Identify the blood parasite species.
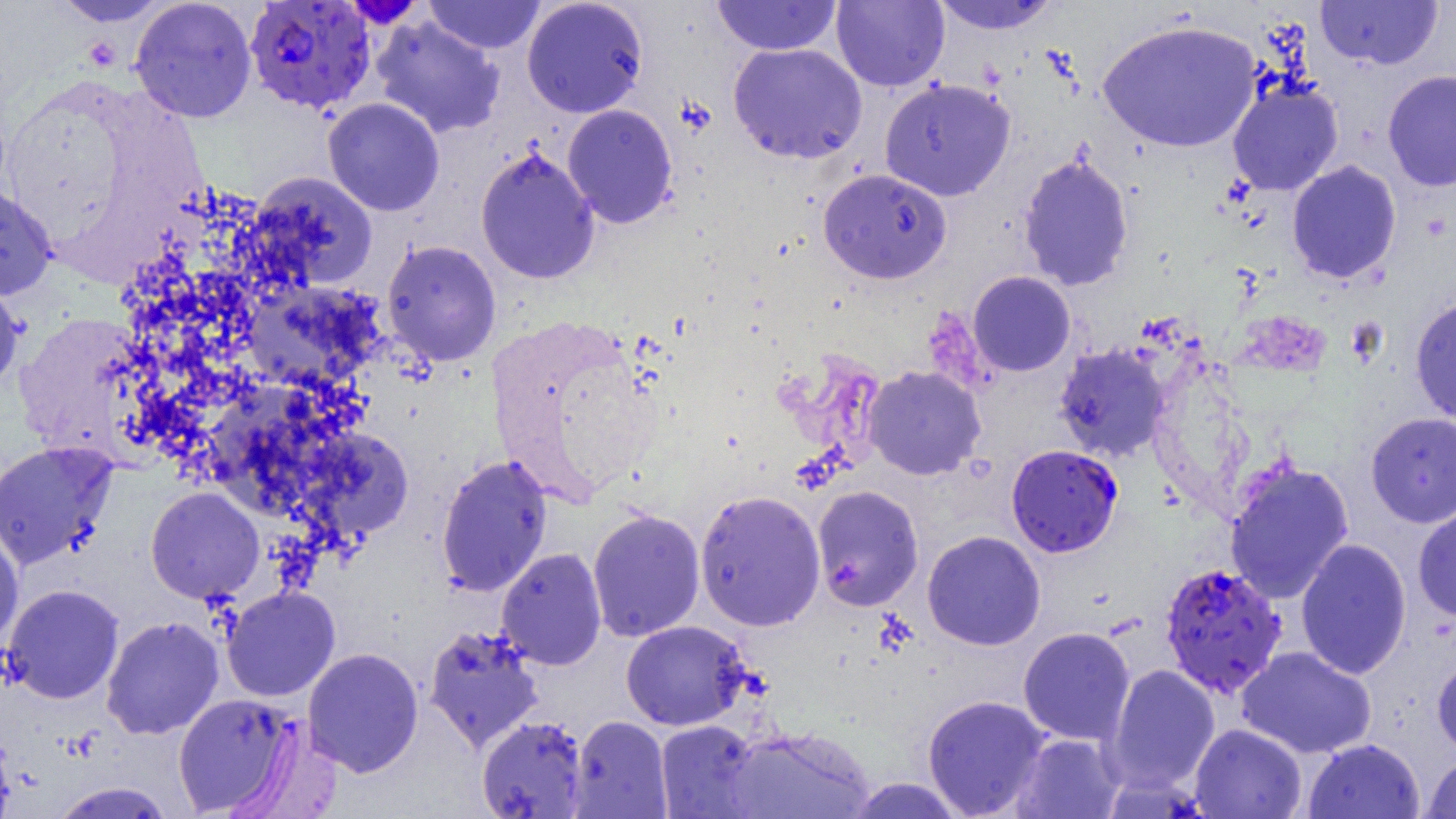

Plasmodium falciparum.

Approximate bounding boxes as (x1,y1)-(x2,y2) corner pairs in pixels. Uninfected red blood cell locations: (51,0)-(172,26), (424,0)-(546,54), (521,0)-(649,118), (711,0)-(842,56), (831,0)-(949,91), (930,0)-(1061,35), (1315,0)-(1443,69), (130,1)-(257,123), (371,16)-(505,138), (1097,19)-(1262,153), (728,43)-(868,164), (1382,70)-(1456,192), (879,77)-(1015,201), (1227,78)-(1343,196), (322,98)-(445,216), (562,104)-(678,228), (475,147)-(600,284), (1017,152)-(1135,292), (1286,160)-(1402,284), (818,168)-(952,283), (249,171)-(378,290), (0,184)-(56,301), (382,240)-(502,365), (968,271)-(1076,376), (0,276)-(26,395), (243,281)-(384,392), (1410,297)-(1456,424), (12,314)-(155,459), (1054,344)-(1171,461), (862,365)-(986,480), (1366,412)-(1456,527), (294,426)-(415,547), (0,441)-(117,569), (435,453)-(553,597), (1224,460)-(1355,605), (811,485)-(924,611), (146,486)-(264,603), (695,489)-(826,631), (1413,505)-(1456,621), (587,508)-(705,641), (0,529)-(23,648), (922,530)-(1045,650), (1295,538)-(1412,680), (496,548)-(607,670), (3,584)-(124,704), (222,586)-(340,702), (101,616)-(224,739), (621,620)-(751,730), (423,624)-(544,753), (1018,626)-(1135,745), (1236,646)-(1377,758), (302,647)-(424,777), (1432,652)-(1456,760), (1104,664)-(1220,794), (173,693)-(299,816), (922,694)-(1051,818), (476,714)-(588,818), (568,715)-(672,818), (655,720)-(765,818), (1189,723)-(1306,819), (0,725)-(15,819), (723,726)-(876,818), (1011,733)-(1125,818), (1303,738)-(1425,819), (1422,753)-(1456,818), (846,777)-(967,818), (50,782)-(176,818). Plasmodium falciparum-infected red blood cell locations: (244,1)-(377,114), (1006,444)-(1123,557), (1159,561)-(1288,698). 1000x magnification. Thin blood film. Optical microscopy. One field of a larger specimen. Image is 1456×819 pixels.